Give the position of every Plasmodium parasite.
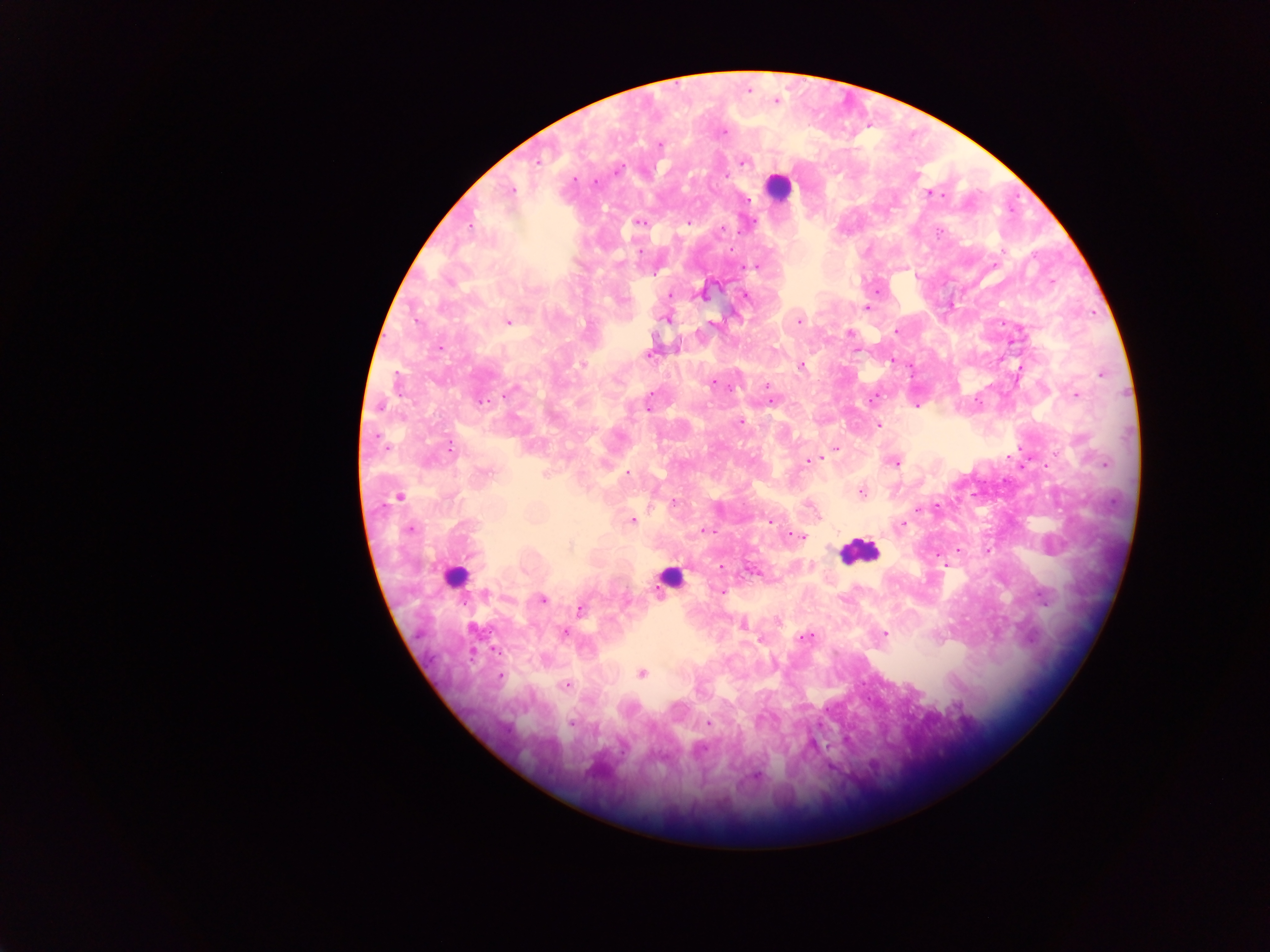
Approximate centers as x y in pixels.
Plasmodium parasites: 747 89; 775 100; 721 131; 659 144; 536 161; 743 161; 594 182; 510 190; 932 193; 749 200; 640 221; 687 222; 720 229; 757 265; 877 290; 702 293; 669 295; 745 296; 867 308; 666 318; 798 320; 508 321; 713 323; 896 330; 849 333; 892 361; 582 364; 800 365; 1018 371; 713 383; 767 385; 1076 394; 771 400; 647 403; 740 422; 877 424; 836 448; 817 458; 809 461; 895 462; 628 473; 861 492; 398 496; 673 503; 917 509; 631 520; 770 520; 900 526; 409 528; 703 530; 800 536; 958 549; 987 551; 947 566; 721 591; 541 599; 579 609; 776 620; 742 623; 563 632; 884 633; 804 637; 641 673; 500 676; 567 684; 571 723; 709 724.

Leukocyte locations: 777 187; 858 552; 455 575; 670 577. Thick blood smear. Photographed through a microscope with a mobile-phone camera. Image is 1270×952 pixels. Collected in Ghana. Single field of view.